Describe the morphology of the erythrocytes.
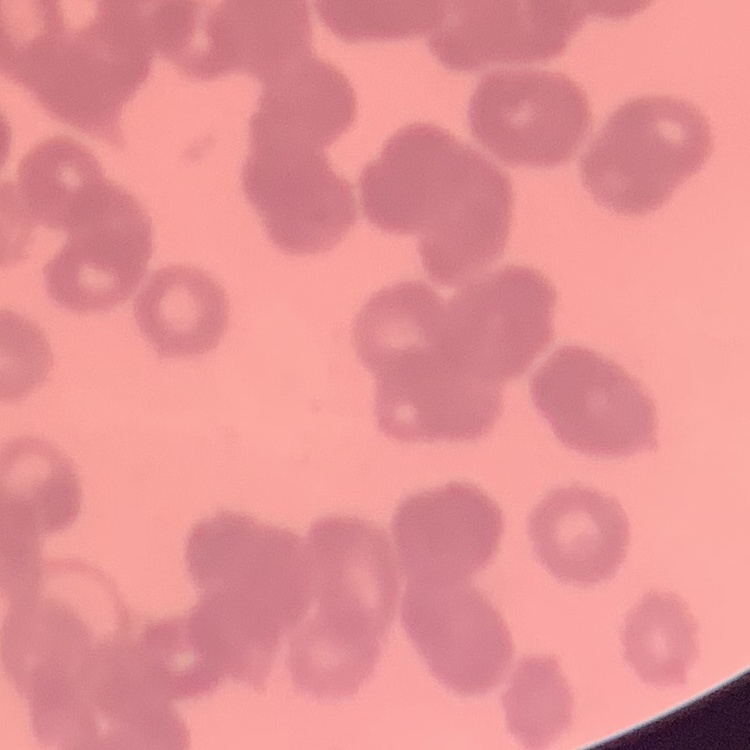

Rouleaux formation.

One tile cut from a larger photomicrograph. Thin blood film. Field's or Giemsa stain.